Classify this cell by malaria status.
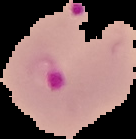
Parasitized.

From a thin blood smear. Image is 136×139 pixels. Cell region segmented out of the field of view; the surrounding area is masked to black.